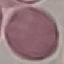
Summary:
  - Malaria status: uninfected
  - Capture: smartphone through the microscope eyepiece
  - Stain: Giemsa
  - Preparation: thin blood smear
  - Image type: cell patch, automatically extracted from a larger field of view and resized to 64 × 64 pixels